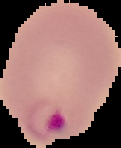 Malaria status: parasitized. Image is 121×148 pixels. From a thin blood film. Cell region segmented out of the field of view; the surrounding area is masked to black.